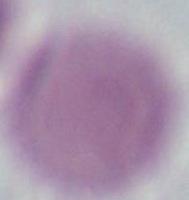
Summary:
  - Modality: photomicrograph
  - Magnification: 1000x
  - Identification: erythrocyte